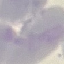

Summary:
  - Result: no malaria parasites seen
  - Preparation: thin blood film
  - Capture: smartphone through the microscope eyepiece
  - Image type: automatically extracted cell patch, resized to 64 × 64 pixels
  - Stain: Giemsa